Point out every malaria parasite.
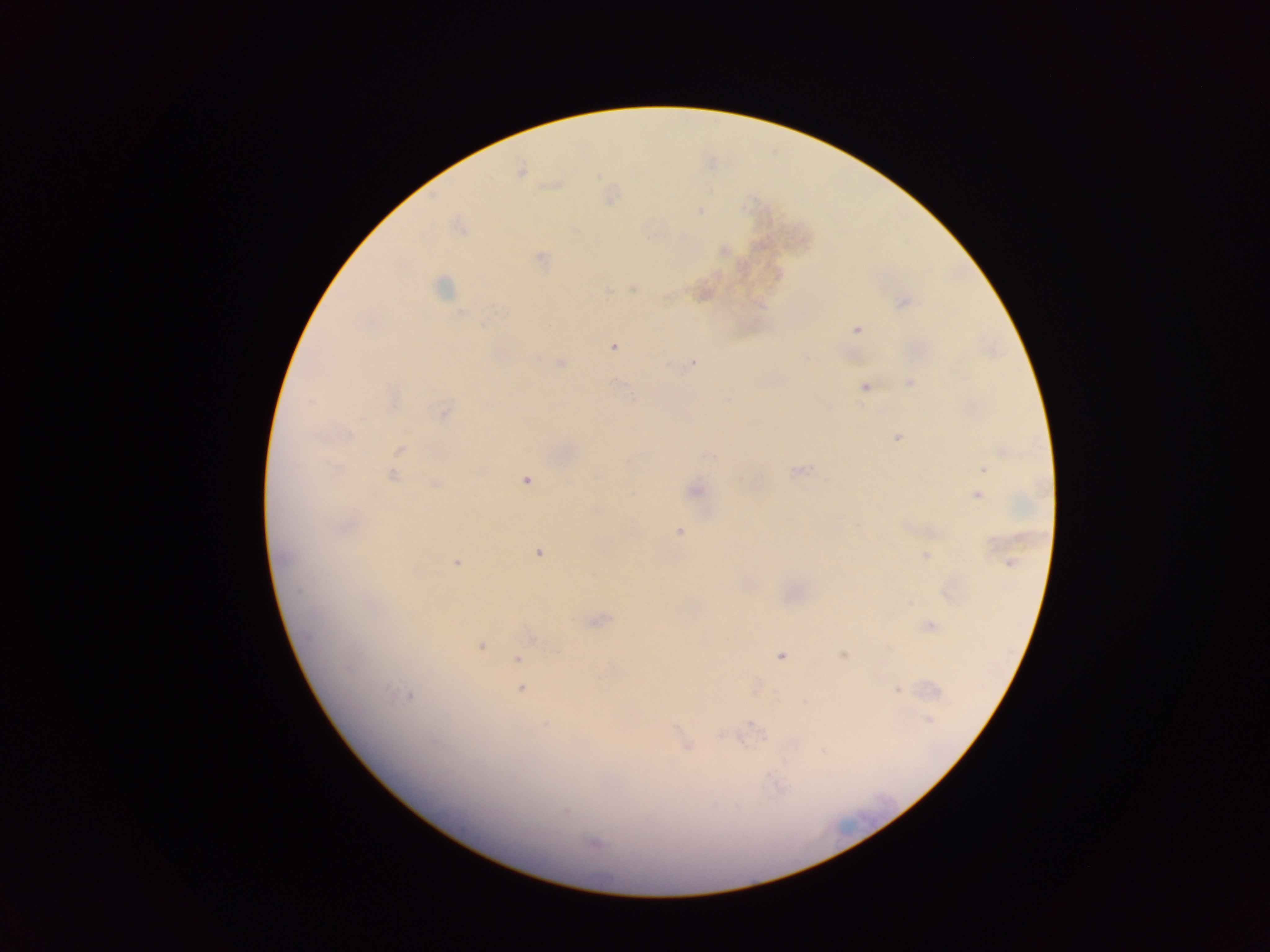
Approximate centers as {x, y} in pixels.
Malaria parasites: {521, 169}, {554, 184}, {610, 195}, {700, 210}, {461, 226}, {574, 230}, {724, 250}, {541, 258}, {443, 288}, {701, 292}, {903, 302}, {857, 329}, {612, 345}, {560, 363}, {692, 363}, {911, 384}, {865, 386}, {394, 399}, {443, 411}, {898, 437}, {399, 451}, {707, 456}, {983, 469}, {797, 470}, {392, 475}, {525, 480}, {434, 484}, {694, 490}, {977, 495}, {679, 532}, {537, 551}, {926, 555}, {455, 561}, {1011, 563}, {949, 592}, {597, 620}, {930, 625}, {479, 645}, {781, 655}, {843, 655}, {518, 659}, {755, 687}, {521, 688}, {898, 689}, {405, 694}, {928, 719}, {544, 724}, {685, 745}, {594, 843}.

Collected in Ghana. Thick blood smear. Mobile-phone photograph taken through the microscope. One field of view. Image is 1270×952 pixels.